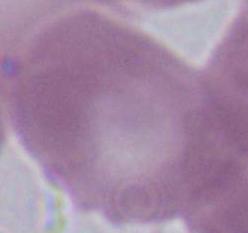

A red blood cell is shown. Captured at 1000x magnification. Micrograph.